Name the parasite shown.
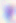

Toxoplasma gondii.

magnification = 400x
modality = photomicrograph